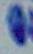 Photomicrograph. 1000x magnification. Toxoplasma gondii is shown.